Name the parasite shown.
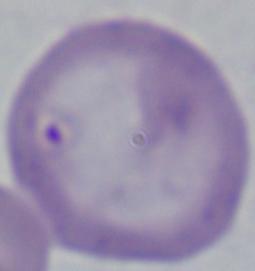

This is Babesia.

magnification = 1000x
modality = micrograph